Give the position of every Plasmodium parasite.
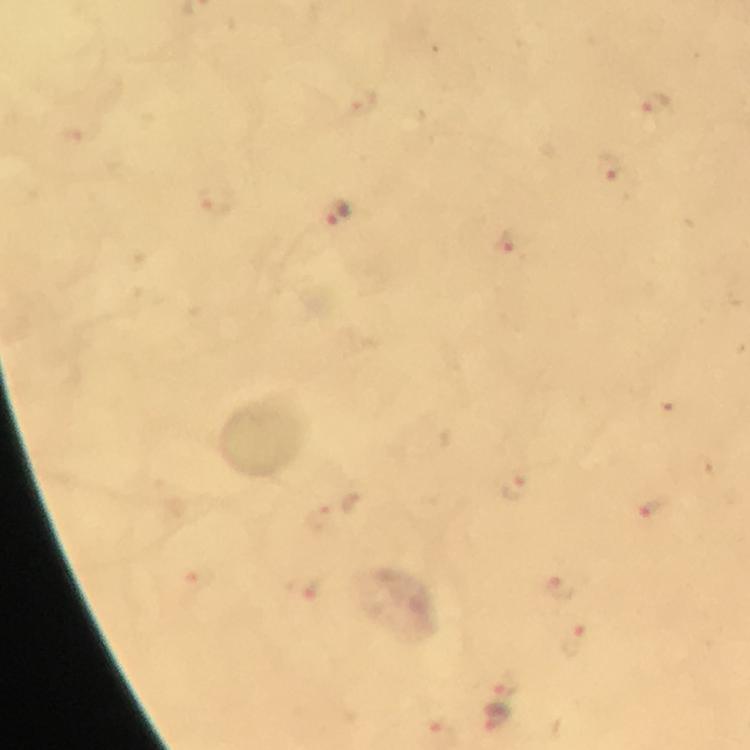

Approximate centers as [x, y] in pixels.
Plasmodium parasites: [657, 105], [608, 168], [337, 216], [506, 245], [515, 485], [653, 506], [559, 586], [301, 588], [575, 643], [507, 686], [497, 718].

{
  "magnification": "100x",
  "immersion_oil": "used",
  "context": "from a malaria diagnostic workup",
  "cropped_from": "one field of view",
  "image_size": "750×750 pixels",
  "stain": "Giemsa",
  "capture": "smartphone photograph through a microscope",
  "preparation": "thick blood film"
}